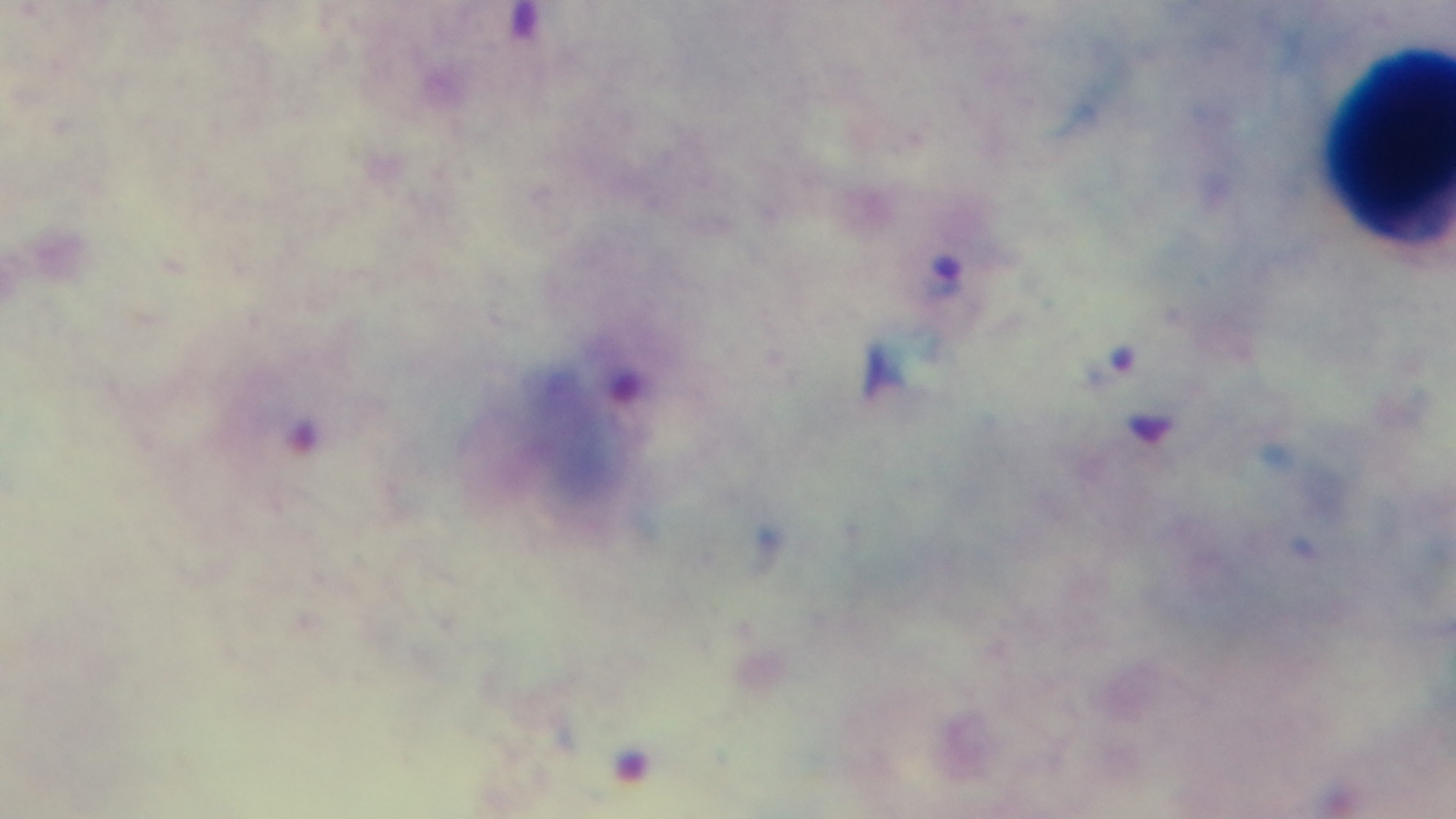 Captured with a mounted 4K digital camera. Malaria status: infected. Photomicrograph. Giemsa-stained. One field from the slide. Preparation: thick blood film. 100x oil-immersion objective.